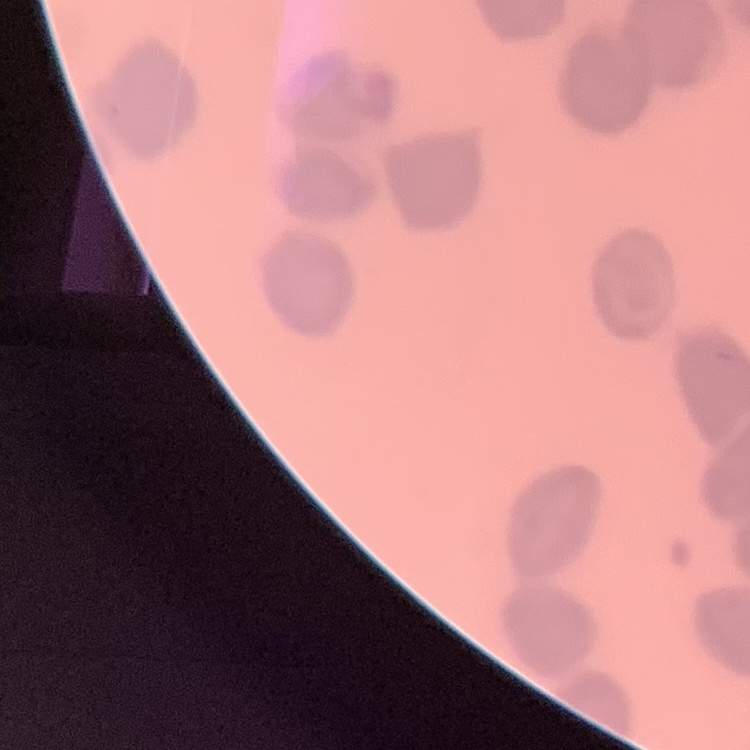
The erythrocytes show no rouleaux formation. One tile cut from a larger photomicrograph. Field's or Giemsa stain. Thin blood smear.